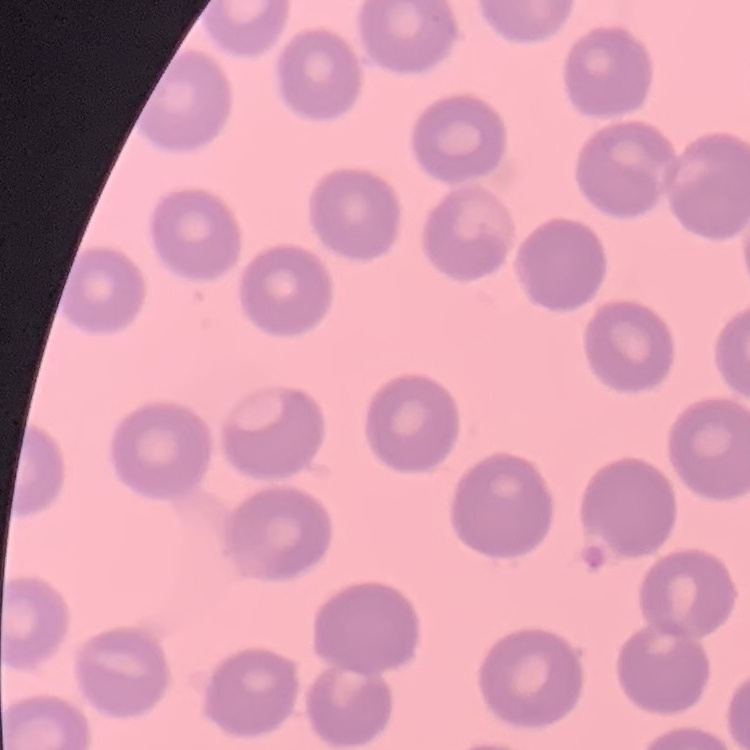 The red blood cells show no rouleaux formation. Square crop of a larger photomicrograph. Thin peripheral smear. Field's or Giemsa stain.